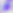

Summary:
  - Magnification: 400x
  - Modality: photomicrograph
  - Identification: Toxoplasma gondii